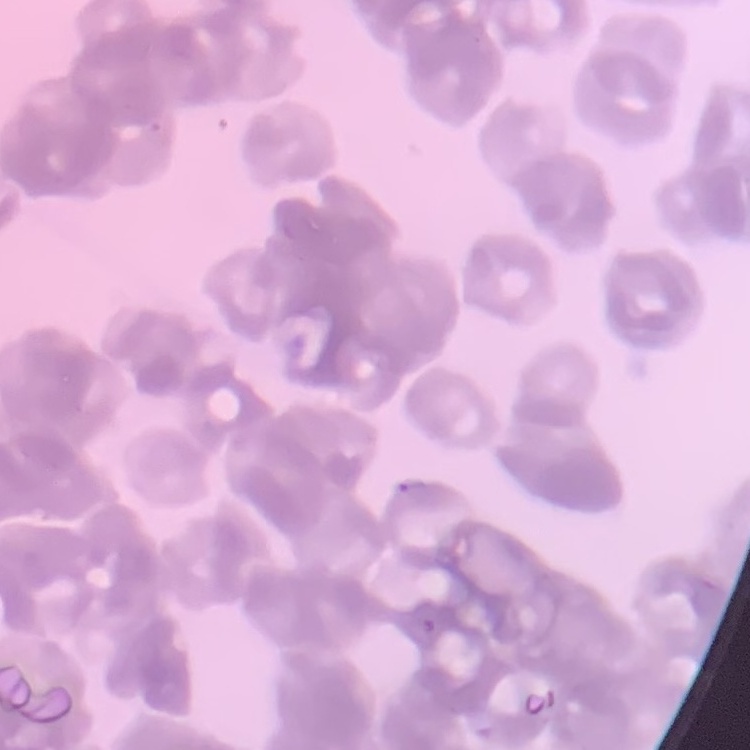
erythrocyte morphology = rouleaux formation
image type = square crop of a larger photomicrograph
preparation = thin blood film
stain = Field's or Giemsa